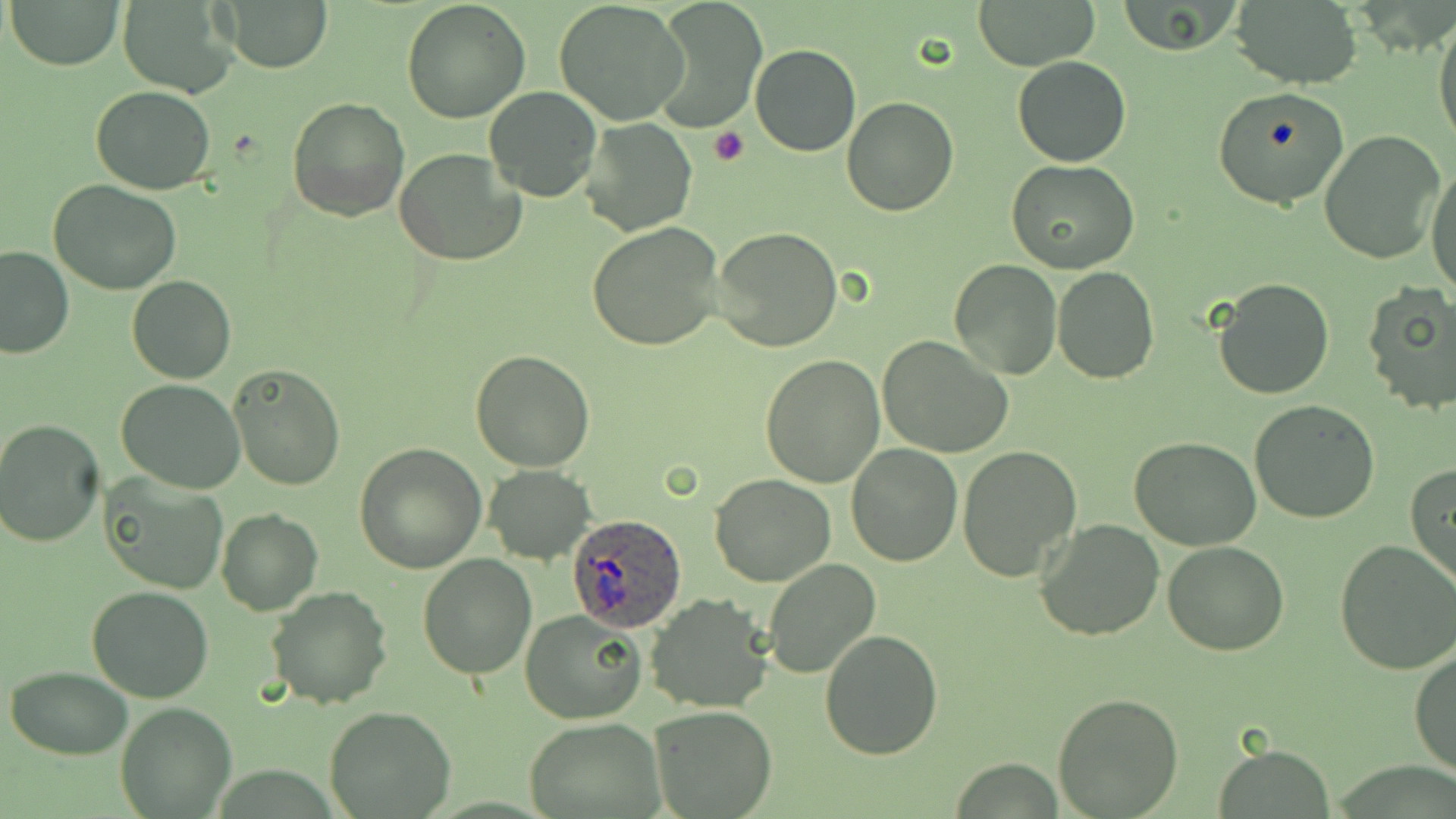
Approximate bounding boxes as (x1, y1, x2, y2) in pixels. Platelet locations: (709, 127, 750, 167). Uninfected red blood cell locations: (9, 0, 124, 70), (217, 0, 334, 72), (401, 0, 531, 122), (553, 0, 689, 125), (973, 0, 1100, 70), (1115, 0, 1241, 56), (649, 2, 768, 131), (1229, 2, 1363, 89), (118, 3, 237, 94), (1432, 16, 1455, 156), (750, 44, 860, 157), (1013, 55, 1130, 167), (789, 69, 926, 193), (482, 86, 601, 203), (1212, 86, 1351, 211), (91, 87, 217, 194), (287, 96, 411, 222), (841, 97, 959, 218), (580, 117, 698, 236), (1317, 130, 1446, 266), (393, 146, 528, 267), (1007, 160, 1138, 274), (1427, 160, 1456, 295), (49, 179, 182, 295), (586, 222, 727, 353), (711, 226, 842, 352), (0, 247, 72, 359), (948, 258, 1062, 381), (1053, 266, 1159, 383), (127, 275, 237, 384), (1212, 277, 1335, 401), (1362, 283, 1456, 415), (878, 336, 1014, 458), (470, 350, 596, 472), (760, 354, 887, 487), (227, 361, 346, 491), (115, 379, 245, 493), (1249, 399, 1381, 523), (1, 419, 105, 546), (1128, 438, 1261, 551), (355, 442, 487, 573), (846, 445, 962, 567), (956, 446, 1083, 582), (1407, 464, 1456, 589), (484, 467, 594, 563), (709, 472, 836, 586), (103, 473, 229, 593), (216, 508, 322, 616), (1035, 519, 1165, 641), (1335, 539, 1456, 674), (1164, 541, 1289, 656), (417, 552, 538, 678), (763, 557, 883, 679), (87, 584, 214, 702), (264, 585, 393, 709), (646, 593, 776, 712), (521, 610, 646, 724), (818, 629, 944, 760), (1411, 650, 1456, 780), (6, 666, 132, 759), (1051, 691, 1184, 817), (116, 702, 237, 818), (323, 705, 458, 819), (650, 705, 777, 818), (524, 716, 663, 817), (1213, 745, 1335, 819). Plasmodium ovale-infected red blood cell locations: (567, 511, 687, 631). Slide-level diagnosis: Plasmodium ovale. 1000x magnification. Single field of view. May-Grünwald-Giemsa stain. Image is 1456×819 pixels. Light microscopy. Thin blood smear.